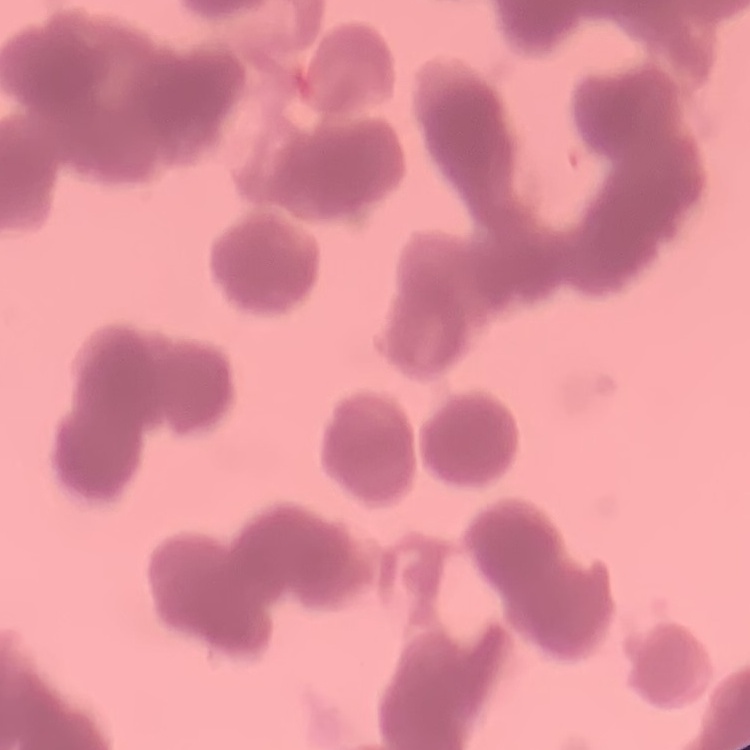
{
  "erythrocyte_morphology": "rouleaux formation",
  "preparation": "thin blood smear",
  "image_type": "square crop of a larger photomicrograph",
  "stain": "Field's or Giemsa"
}